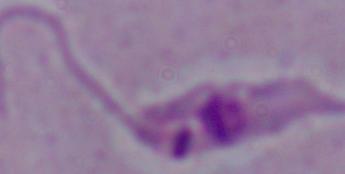

Summary:
  - Magnification: 1000x
  - Identification: Leishmania
  - Modality: photomicrograph